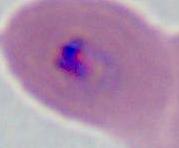

Captured at either 400x or 1000x magnification. Photomicrograph. A Plasmodium parasite is seen.